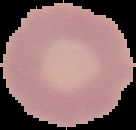

Summary:
  - Result: no Plasmodium parasites detected
  - Image type: segmented cell region on a black background
  - Image size: 136×130 pixels
  - Preparation: thin blood film